Locate Plasmodium parasites and leukocytes.
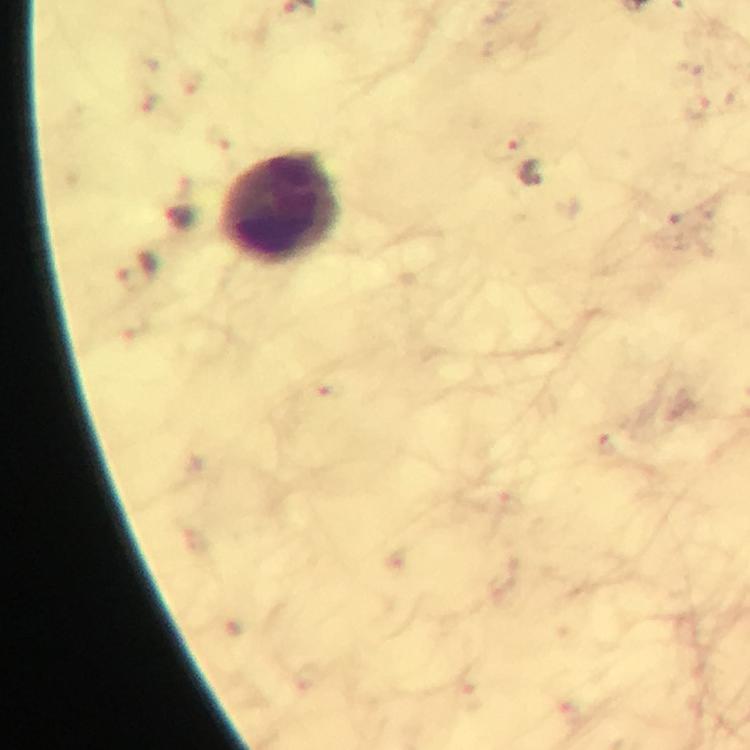
Approximate centers as (x, y) in pixels.
Plasmodium parasites: (503, 146).
Leukocytes: (277, 207).

{
  "immersion_oil": "used",
  "image_size": "750×750 pixels",
  "cropped_from": "a single field of view",
  "context": "from a diagnostic examination for malaria",
  "stain": "Giemsa",
  "magnification": "100x",
  "capture": "smartphone camera through the microscope",
  "preparation": "thick blood film"
}